Give the extent of all Babesia divergens-infected red blood cells.
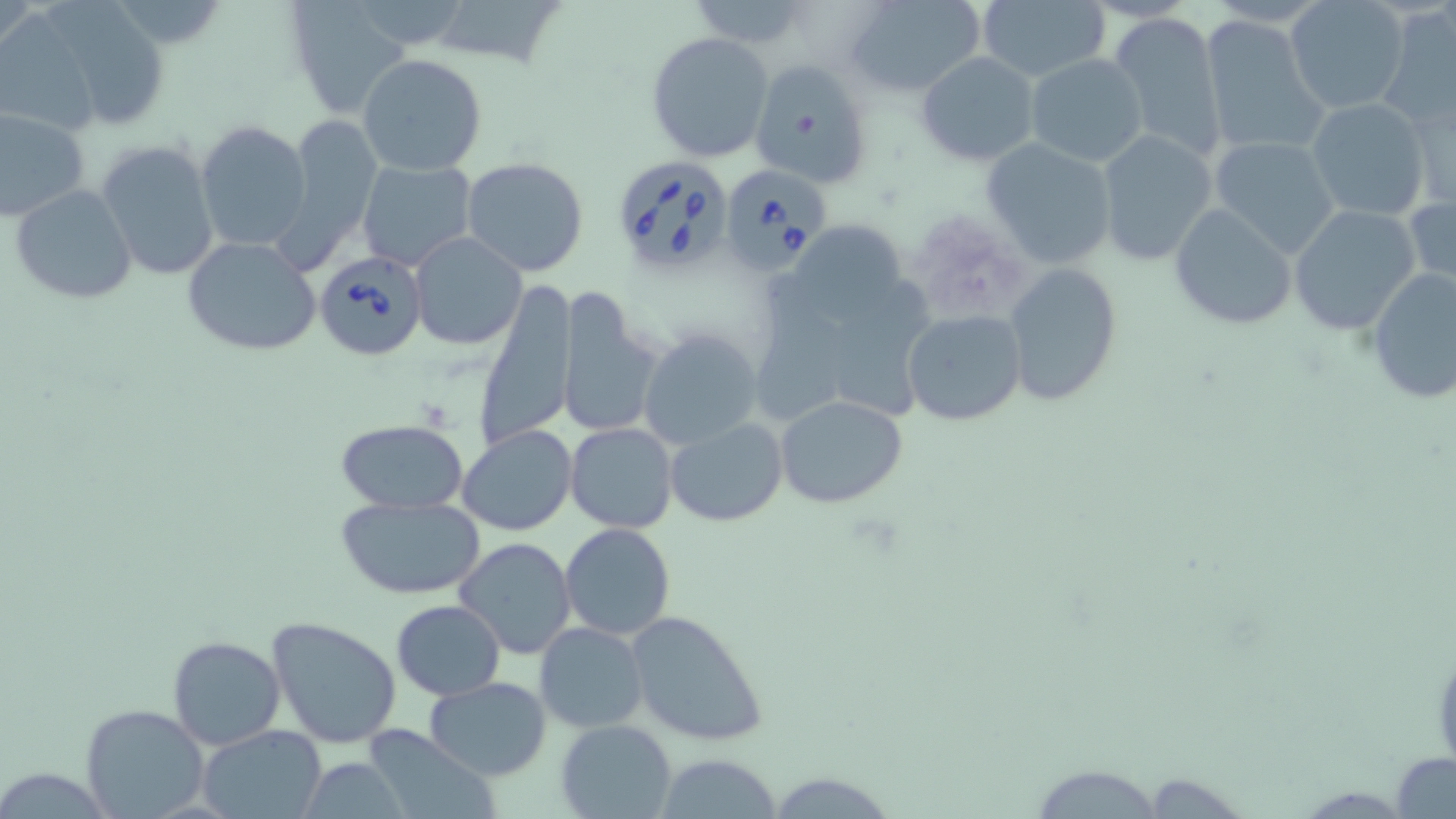

Approximate bounding boxes as named x1/y1/x2/y2 corners in pixels.
Babesia divergens-infected red blood cells: (x1=609, y1=156, x2=736, y2=275), (x1=716, y1=163, x2=830, y2=276), (x1=314, y1=251, x2=429, y2=361).

Uninfected red blood cell locations: (x1=283, y1=0, x2=409, y2=119), (x1=426, y1=0, x2=568, y2=70), (x1=843, y1=0, x2=986, y2=96), (x1=974, y1=0, x2=1112, y2=85), (x1=680, y1=1, x2=815, y2=46), (x1=1284, y1=1, x2=1410, y2=115), (x1=43, y1=3, x2=171, y2=130), (x1=1379, y1=5, x2=1456, y2=131), (x1=1107, y1=11, x2=1228, y2=160), (x1=1200, y1=15, x2=1328, y2=156), (x1=647, y1=31, x2=776, y2=163), (x1=916, y1=52, x2=1038, y2=166), (x1=1026, y1=53, x2=1146, y2=167), (x1=357, y1=54, x2=488, y2=176), (x1=748, y1=58, x2=872, y2=189), (x1=1010, y1=75, x2=1141, y2=243), (x1=1406, y1=88, x2=1454, y2=210), (x1=1305, y1=96, x2=1432, y2=222), (x1=0, y1=106, x2=90, y2=222), (x1=281, y1=113, x2=383, y2=261), (x1=195, y1=120, x2=312, y2=254), (x1=1094, y1=129, x2=1218, y2=267), (x1=1210, y1=136, x2=1342, y2=258), (x1=979, y1=138, x2=1117, y2=269), (x1=95, y1=140, x2=220, y2=282), (x1=357, y1=159, x2=480, y2=273), (x1=461, y1=159, x2=590, y2=277), (x1=9, y1=184, x2=138, y2=305), (x1=1405, y1=190, x2=1456, y2=301), (x1=1169, y1=202, x2=1297, y2=331), (x1=1286, y1=203, x2=1424, y2=337), (x1=408, y1=232, x2=527, y2=350), (x1=181, y1=236, x2=324, y2=357), (x1=1004, y1=263, x2=1122, y2=405), (x1=1365, y1=265, x2=1456, y2=409), (x1=476, y1=277, x2=578, y2=454), (x1=553, y1=290, x2=664, y2=441), (x1=904, y1=310, x2=1025, y2=426), (x1=637, y1=327, x2=763, y2=449), (x1=776, y1=395, x2=909, y2=509), (x1=335, y1=418, x2=468, y2=515), (x1=665, y1=418, x2=787, y2=527), (x1=566, y1=422, x2=678, y2=533), (x1=457, y1=424, x2=579, y2=535), (x1=336, y1=495, x2=486, y2=600), (x1=559, y1=523, x2=675, y2=641), (x1=455, y1=537, x2=578, y2=659), (x1=392, y1=600, x2=505, y2=699), (x1=624, y1=608, x2=769, y2=747), (x1=266, y1=615, x2=403, y2=750), (x1=535, y1=622, x2=649, y2=732), (x1=169, y1=634, x2=284, y2=749), (x1=424, y1=676, x2=550, y2=780), (x1=81, y1=703, x2=209, y2=818), (x1=555, y1=719, x2=677, y2=818), (x1=196, y1=725, x2=327, y2=819), (x1=360, y1=725, x2=499, y2=819), (x1=1389, y1=752, x2=1456, y2=818), (x1=653, y1=755, x2=787, y2=817), (x1=1025, y1=763, x2=1172, y2=817). Slide-level diagnosis: Babesia divergens. Image is 1456×819 pixels. Light microscopy. Thin blood film. Single field of view. May-Grünwald-Giemsa stain. 1000x magnification.